Report the malaria status of this cell.
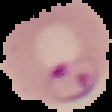
Parasitized.

Image is 112×112 pixels. Segmented cell region on a black background. From a thin blood smear.